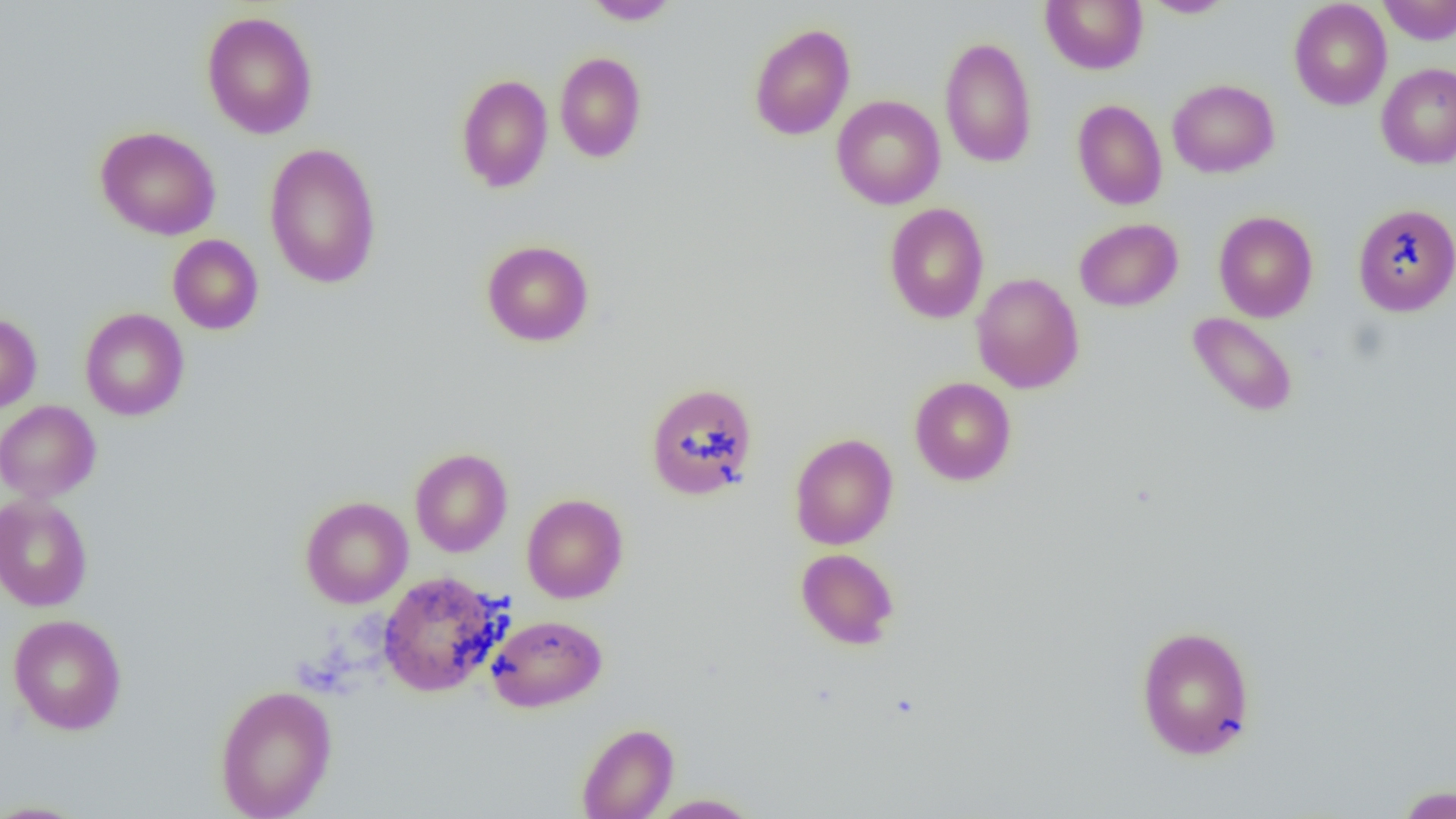
Approximate bounding boxes as [x1, y1, x2, y2] in pixels. Uninfected red blood cell locations: [1041, 0, 1148, 74], [1378, 0, 1456, 45], [583, 1, 681, 25], [1141, 1, 1237, 18], [1288, 1, 1392, 110], [201, 11, 319, 139], [749, 23, 855, 140], [939, 36, 1037, 168], [554, 52, 647, 163], [1376, 62, 1456, 169], [455, 74, 553, 193], [1167, 79, 1280, 178], [832, 95, 945, 209], [1072, 99, 1167, 210], [95, 126, 222, 240], [264, 143, 382, 289], [1353, 202, 1456, 316], [884, 203, 989, 324], [1213, 210, 1319, 322], [1074, 218, 1183, 311], [168, 234, 264, 335], [481, 240, 594, 346], [971, 272, 1084, 393], [80, 308, 189, 421], [1187, 311, 1299, 418], [0, 313, 42, 413], [909, 377, 1017, 485], [645, 382, 759, 500], [0, 400, 101, 502], [789, 432, 898, 550], [410, 448, 512, 557], [0, 493, 93, 612], [522, 493, 628, 603], [300, 496, 413, 608], [796, 548, 900, 649], [377, 571, 507, 698], [8, 614, 127, 735], [486, 614, 607, 713], [1135, 624, 1256, 761], [214, 684, 337, 819], [577, 723, 679, 818], [1393, 784, 1455, 819], [648, 793, 762, 818], [0, 800, 90, 818]. Slide-level diagnosis: no evidence of blood parasites. Thin blood film. 1000x magnification. Image is 1456×819 pixels. Optical microscopy. One field of a larger specimen.